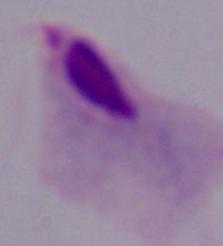
modality = photomicrograph
identification = trichomonad
magnification = 1000x